Identify the parasite.
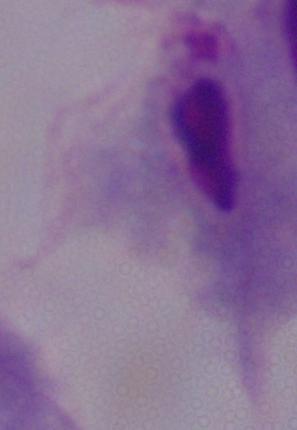

A trichomonad.

Captured at 1000x magnification. Photomicrograph.